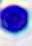 A white blood cell is seen. 400x magnification. Micrograph.